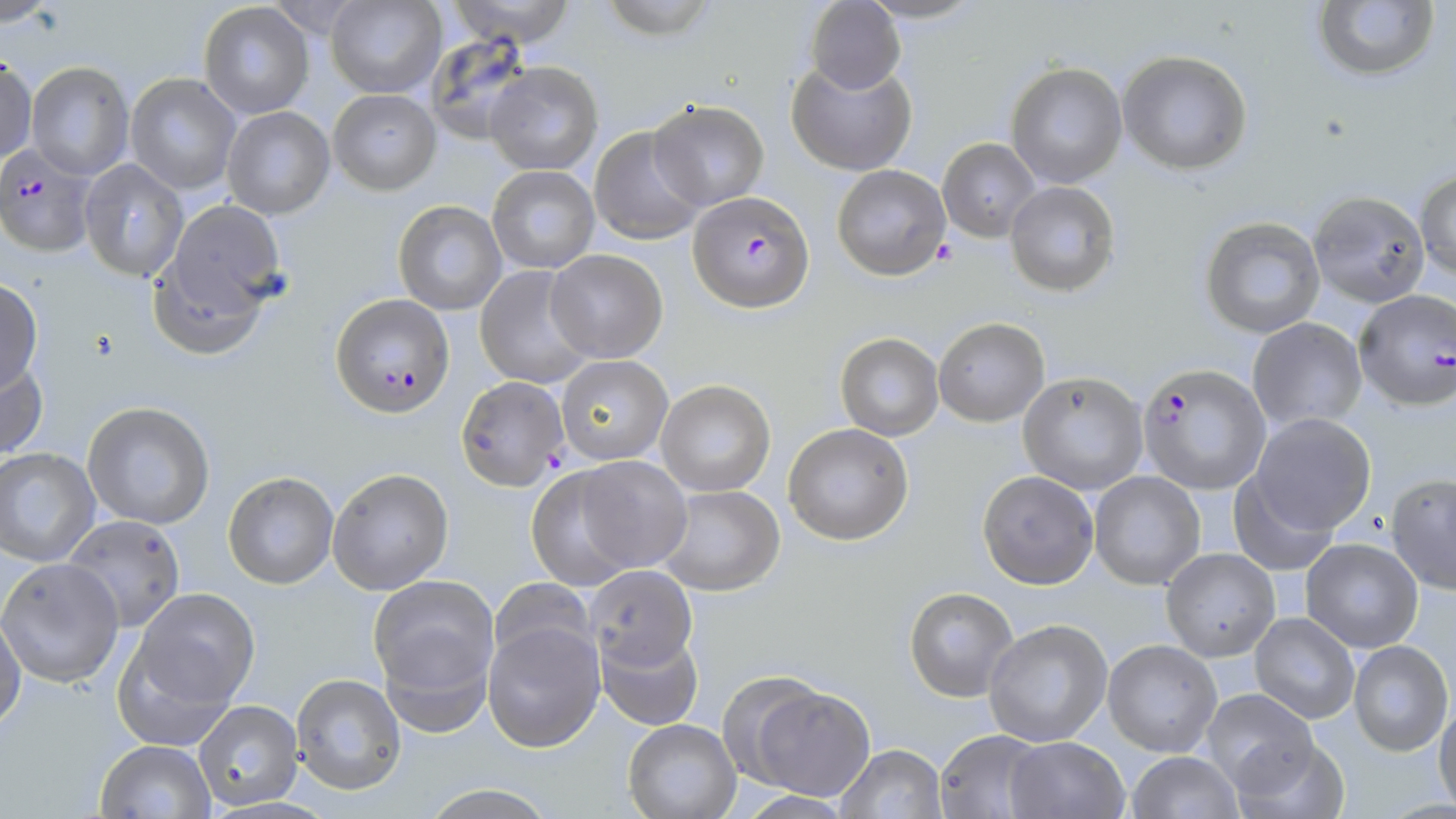
{
  "slide_level_diagnosis": "Plasmodium falciparum",
  "modality": "light microscopy",
  "plasmodium_falciparum_infected_red_blood_cell_locations": "approximate bounding boxes as (x1, y1, x2, y2) in pixels: (0, 145, 97, 259), (688, 192, 814, 316), (1354, 291, 1456, 414), (330, 294, 455, 420), (1138, 366, 1270, 496)",
  "stain": "May-Grünwald-Giemsa",
  "image_size": "1456×819 pixels",
  "field_of_view": "one of a larger specimen",
  "magnification": "1000x",
  "preparation": "thin blood smear",
  "uninfected_red_blood_cell_locations": "approximate bounding boxes as (x1, y1, x2, y2) in pixels: (0, 0, 61, 28), (325, 0, 447, 98), (446, 0, 578, 47), (596, 0, 722, 44), (1311, 0, 1442, 86), (805, 1, 906, 96), (198, 2, 315, 119), (425, 34, 538, 145), (1117, 54, 1253, 180), (0, 57, 37, 163), (785, 59, 917, 177), (26, 61, 134, 180), (484, 62, 603, 174), (1005, 64, 1128, 190), (124, 72, 241, 195), (327, 89, 442, 195), (648, 101, 770, 211), (222, 107, 335, 220), (589, 126, 706, 247), (938, 139, 1041, 244), (78, 158, 189, 283), (487, 165, 600, 274), (831, 166, 951, 284), (1415, 171, 1456, 282), (1004, 183, 1121, 300), (1308, 193, 1430, 310), (392, 200, 506, 315), (161, 201, 287, 327), (1200, 218, 1326, 340), (147, 246, 269, 360), (545, 250, 668, 363), (474, 266, 595, 389), (0, 278, 43, 396), (1247, 319, 1367, 432), (933, 320, 1050, 429), (834, 334, 944, 441), (556, 355, 673, 466), (0, 357, 49, 462), (1017, 375, 1148, 495), (455, 377, 569, 492), (656, 380, 775, 496), (82, 401, 215, 530), (1249, 415, 1376, 537), (782, 424, 913, 547), (0, 448, 100, 567), (573, 456, 692, 574), (327, 469, 454, 596), (525, 469, 641, 590), (223, 472, 339, 591), (1089, 472, 1205, 592), (977, 473, 1099, 593), (1227, 473, 1339, 574), (1386, 475, 1456, 596), (656, 486, 785, 597), (62, 515, 186, 633), (1300, 541, 1423, 654), (1160, 550, 1280, 664), (0, 559, 124, 688), (585, 566, 698, 673), (368, 575, 499, 707), (489, 579, 596, 673), (903, 588, 1018, 704), (130, 590, 261, 715), (0, 612, 26, 737), (1249, 614, 1360, 724), (482, 619, 605, 753), (984, 621, 1113, 748), (595, 628, 704, 731), (112, 637, 239, 751), (1103, 642, 1222, 758), (1348, 642, 1453, 758), (290, 674, 407, 797), (742, 681, 875, 800), (1203, 690, 1319, 800), (194, 700, 304, 811), (1433, 701, 1456, 815), (623, 719, 741, 818), (934, 730, 1050, 819), (1004, 738, 1129, 819), (1232, 739, 1349, 818), (94, 741, 215, 818), (836, 745, 947, 819), (1126, 752, 1244, 819), (420, 784, 559, 819), (736, 790, 853, 818)"
}